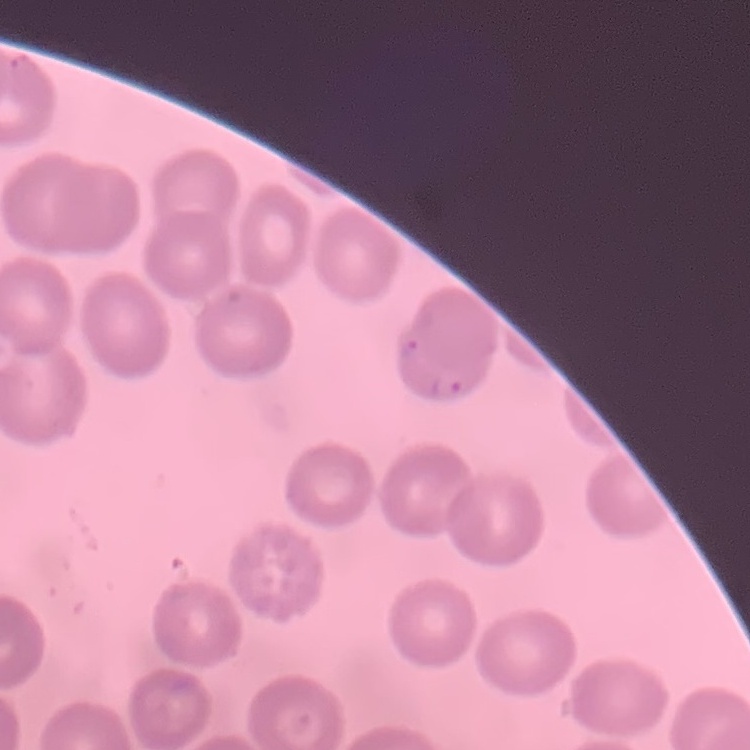
red blood cell morphology = no rouleaux formation
image type = square crop of a larger photomicrograph
preparation = thin peripheral smear
stain = Field's or Giemsa